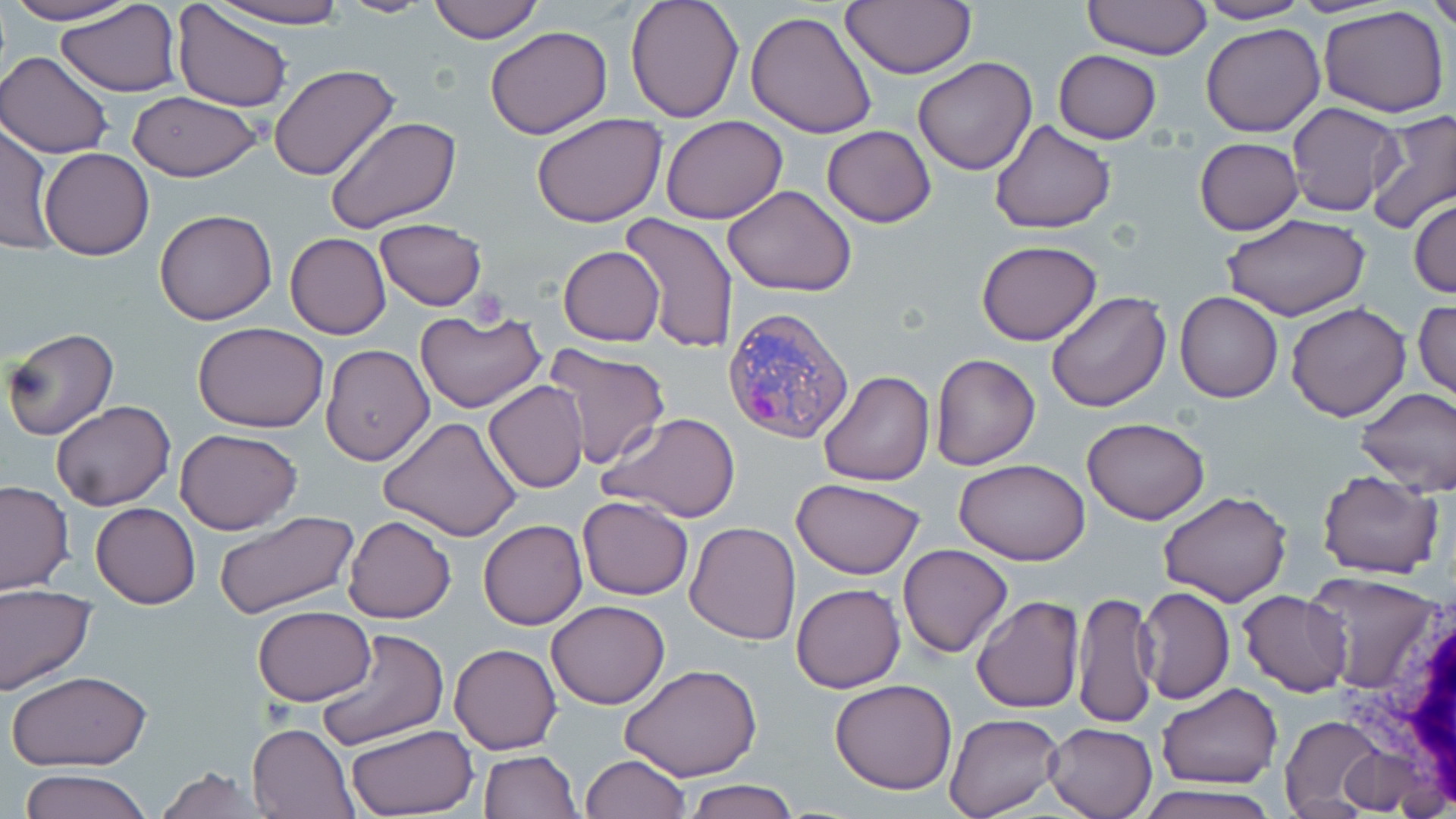
Plasmodium vivax-infected red blood cell locations = approximate bounding boxes as [x1, y1, x2, y2] in pixels: [721, 306, 855, 443]
slide-level diagnosis = Plasmodium vivax
white blood cell locations = approximate bounding boxes as [x1, y1, x2, y2] in pixels: [1346, 584, 1456, 814]
stain = May-Grünwald-Giemsa
field of view = single
platelet locations = approximate bounding boxes as [x1, y1, x2, y2] in pixels: [464, 287, 508, 325]
image size = 1456×819 pixels
modality = light microscopy
uninfected red blood cell locations = approximate bounding boxes as [x1, y1, x2, y2] in pixels: [2, 0, 136, 25], [203, 0, 354, 29], [334, 0, 436, 17], [426, 0, 544, 43], [625, 0, 744, 120], [1082, 0, 1210, 59], [1429, 0, 1456, 33], [840, 1, 976, 79], [1193, 1, 1311, 23], [56, 2, 181, 96], [172, 2, 294, 113], [1319, 5, 1449, 118], [745, 9, 878, 140], [1202, 21, 1325, 137], [484, 26, 612, 139], [1054, 50, 1162, 143], [0, 53, 113, 158], [913, 56, 1037, 174], [268, 64, 402, 184], [127, 92, 262, 181], [1286, 102, 1405, 217], [532, 111, 667, 227], [1365, 111, 1456, 235], [660, 115, 788, 224], [324, 116, 462, 236], [0, 118, 54, 255], [989, 121, 1115, 234], [822, 125, 936, 228], [1195, 137, 1304, 234], [39, 148, 156, 260], [723, 185, 858, 297], [1410, 198, 1456, 299], [154, 208, 279, 326], [619, 214, 738, 353], [1221, 214, 1370, 320], [375, 219, 488, 310], [285, 233, 391, 338], [977, 241, 1102, 346], [558, 245, 665, 346], [1047, 290, 1171, 413], [1175, 291, 1283, 403], [1414, 298, 1455, 400], [1286, 302, 1412, 421], [416, 309, 546, 415], [193, 321, 330, 433], [3, 326, 119, 439], [544, 341, 672, 470], [321, 345, 434, 465], [930, 352, 1040, 469], [818, 369, 934, 487], [483, 380, 590, 493], [1357, 386, 1456, 495], [49, 400, 176, 512], [598, 413, 742, 523], [377, 416, 524, 541], [1083, 418, 1210, 524], [174, 428, 302, 535], [954, 458, 1091, 567], [1317, 469, 1444, 579], [792, 477, 926, 579], [0, 481, 74, 595], [1157, 491, 1292, 607], [577, 497, 693, 600], [91, 503, 200, 608], [212, 509, 359, 622], [343, 515, 455, 624], [478, 518, 587, 630], [685, 521, 800, 646], [898, 543, 1013, 658], [1302, 570, 1443, 695], [0, 582, 96, 695], [791, 582, 905, 693], [1136, 586, 1234, 705], [1237, 589, 1351, 695], [1072, 591, 1158, 728], [971, 596, 1083, 714], [545, 600, 670, 709], [251, 606, 376, 706], [313, 629, 448, 748], [449, 642, 563, 754], [620, 663, 764, 783], [5, 670, 155, 771], [829, 679, 957, 794], [1157, 683, 1281, 789], [945, 713, 1065, 819], [1279, 715, 1389, 814], [247, 721, 359, 818], [1043, 721, 1158, 818], [346, 724, 477, 816], [1337, 747, 1425, 813], [478, 750, 580, 818], [578, 754, 690, 819], [152, 765, 269, 818], [17, 770, 151, 819], [679, 779, 800, 818], [1135, 783, 1285, 819]
magnification = 1000x
preparation = thin blood film